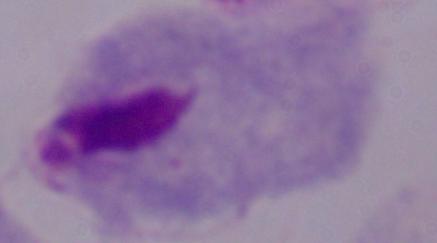
Summary:
  - Magnification: 1000x
  - Modality: photomicrograph
  - Identification: trichomonad